Name the cell type shown.
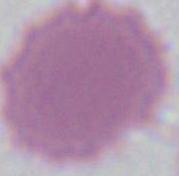
An erythrocyte.

Micrograph. Captured at 1000x magnification.